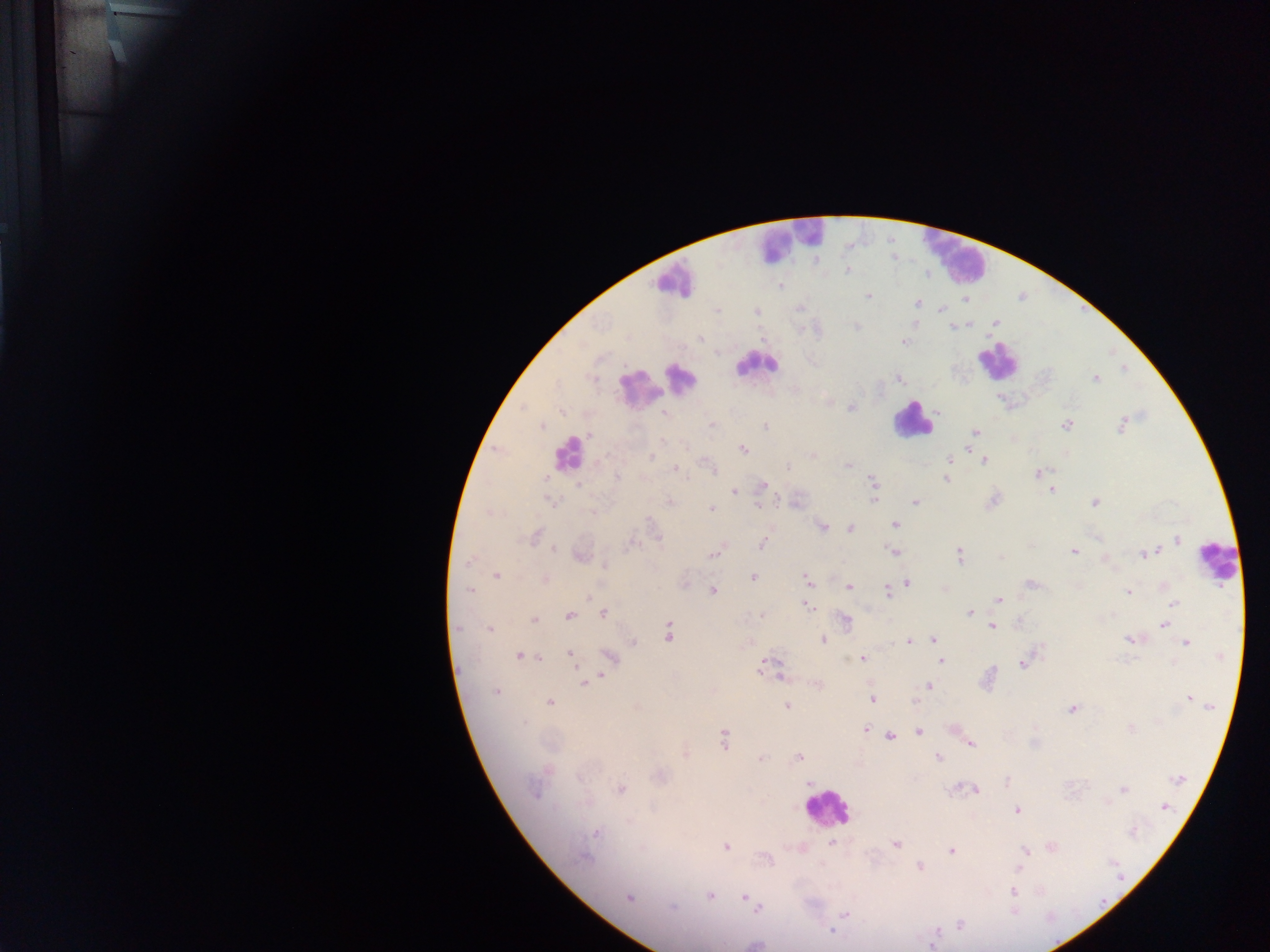

Approximate centers as (x, y) in pixels. Leukocyte locations: (788, 240), (953, 256), (671, 279), (996, 360), (757, 363), (681, 377), (638, 388), (913, 420), (568, 453), (1217, 562), (826, 808). Plasmodium parasite locations: (847, 270), (781, 286), (868, 296), (965, 300), (917, 303), (940, 309), (716, 310), (756, 311), (995, 322), (857, 326), (700, 339), (905, 342), (1095, 378), (900, 380), (852, 407), (562, 412), (665, 414), (712, 425), (1122, 425), (542, 426), (1066, 426), (765, 427), (976, 432), (589, 435), (663, 441), (685, 446), (742, 449), (813, 455), (651, 458), (949, 460), (984, 461), (847, 465), (787, 468), (675, 469), (713, 469), (1039, 473), (618, 477), (545, 478), (946, 478), (873, 483), (579, 485), (762, 485), (733, 491), (1051, 491), (874, 498), (551, 501), (992, 501), (670, 502), (915, 502), (1094, 502), (758, 506), (711, 509), (593, 512), (895, 524), (822, 526), (850, 528), (536, 536), (1177, 540), (630, 544), (762, 544), (553, 550), (892, 551), (1074, 552), (1149, 553), (713, 554), (959, 555), (580, 557), (1001, 557), (1105, 559), (467, 563), (604, 566), (497, 575), (753, 577), (544, 579), (806, 580), (908, 583), (685, 584), (1031, 585), (849, 587), (1166, 587), (469, 590), (713, 591), (887, 592), (1128, 592), (589, 596), (998, 600), (1172, 604), (807, 606), (603, 613), (969, 613), (761, 615), (569, 616), (533, 619), (845, 621), (1019, 623), (992, 625), (1164, 625), (458, 627), (489, 629), (668, 633), (1130, 639), (823, 640), (933, 640), (908, 641), (634, 642), (1187, 643), (570, 654), (519, 656), (1221, 656), (609, 657), (539, 658), (861, 659), (941, 661), (766, 663), (1022, 665), (760, 670), (601, 675), (781, 677), (816, 683), (584, 684), (929, 686), (496, 692), (1189, 699), (872, 700), (916, 701), (551, 702), (1210, 705), (638, 706), (786, 706), (1072, 709), (525, 723), (1131, 728), (866, 730), (919, 732), (891, 736), (724, 738), (971, 744), (685, 755), (798, 757), (938, 758), (760, 759), (661, 777), (1177, 778), (809, 782), (1007, 782), (621, 789), (1123, 789), (974, 790), (534, 793), (1165, 807), (1017, 811), (630, 821), (596, 832), (1132, 832), (832, 843), (895, 844), (726, 847), (1052, 847), (642, 848), (951, 850), (1024, 851), (584, 858), (920, 866), (1020, 867), (1013, 891), (710, 895), (629, 897), (744, 898), (673, 908), (758, 908), (1013, 911), (845, 913), (959, 925), (833, 930), (937, 932), (932, 945). Mobile-phone photograph taken through the microscope. Image is 1270×952 pixels. Thick blood film. Sample from Ghana. Single field of view.